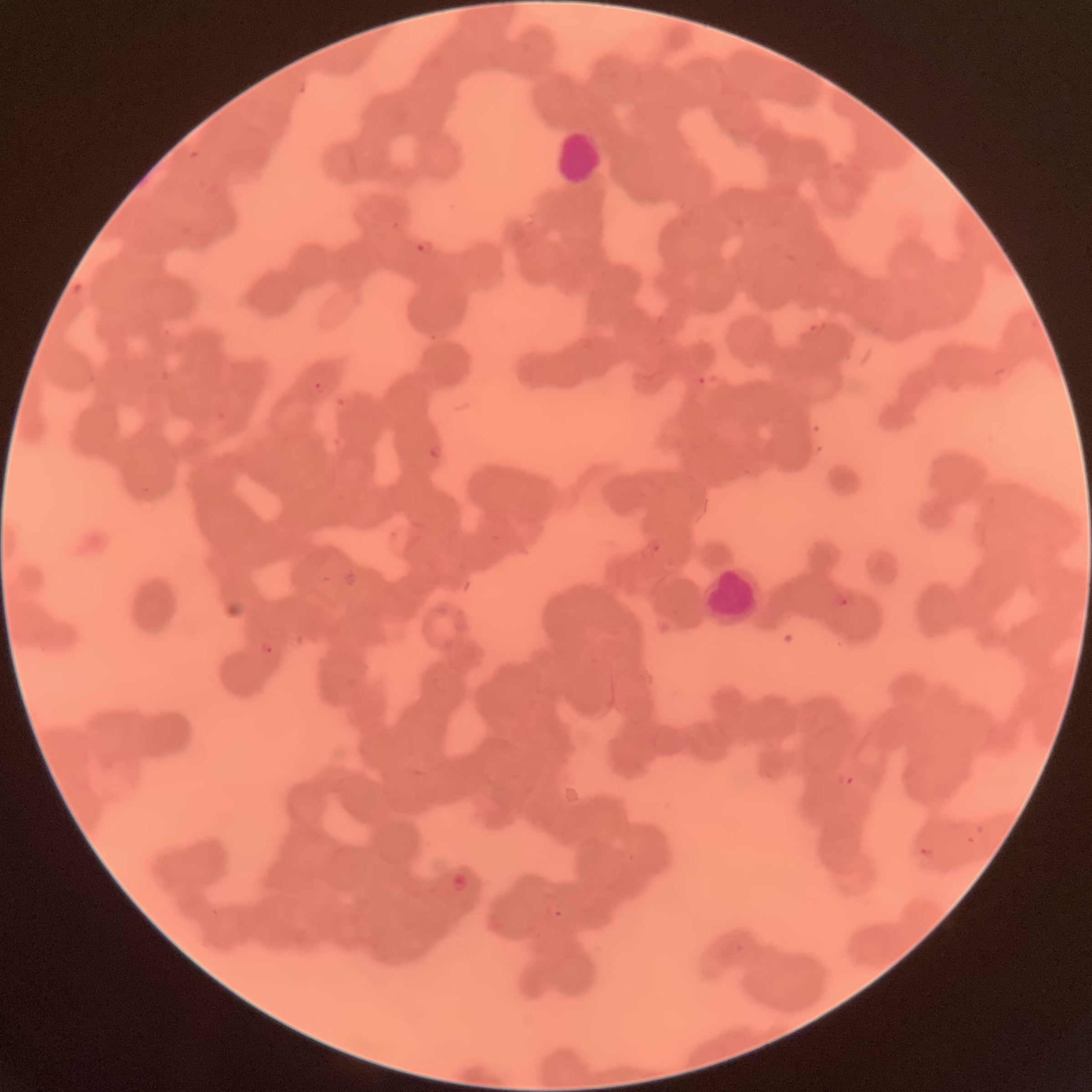
Summary:
  - Coordinate format: approximate bounding boxes as (x1, y1, x2, y2) in pixels
  - White blood cell locations: (552, 129, 603, 183), (703, 563, 761, 624)
  - Plasmodium parasite locations: (415, 238, 434, 256), (313, 378, 330, 394), (429, 443, 441, 459), (639, 537, 663, 560), (831, 591, 855, 609), (259, 639, 275, 656), (836, 770, 855, 788), (916, 845, 936, 860), (618, 850, 633, 863), (449, 873, 469, 893), (544, 901, 568, 921)
  - Preparation: thin blood smear
  - Modality: optical microscopy
  - Red blood cell morphology: rouleaux formation
  - Image size: 1092×1092 pixels